Identify the blood parasite species.
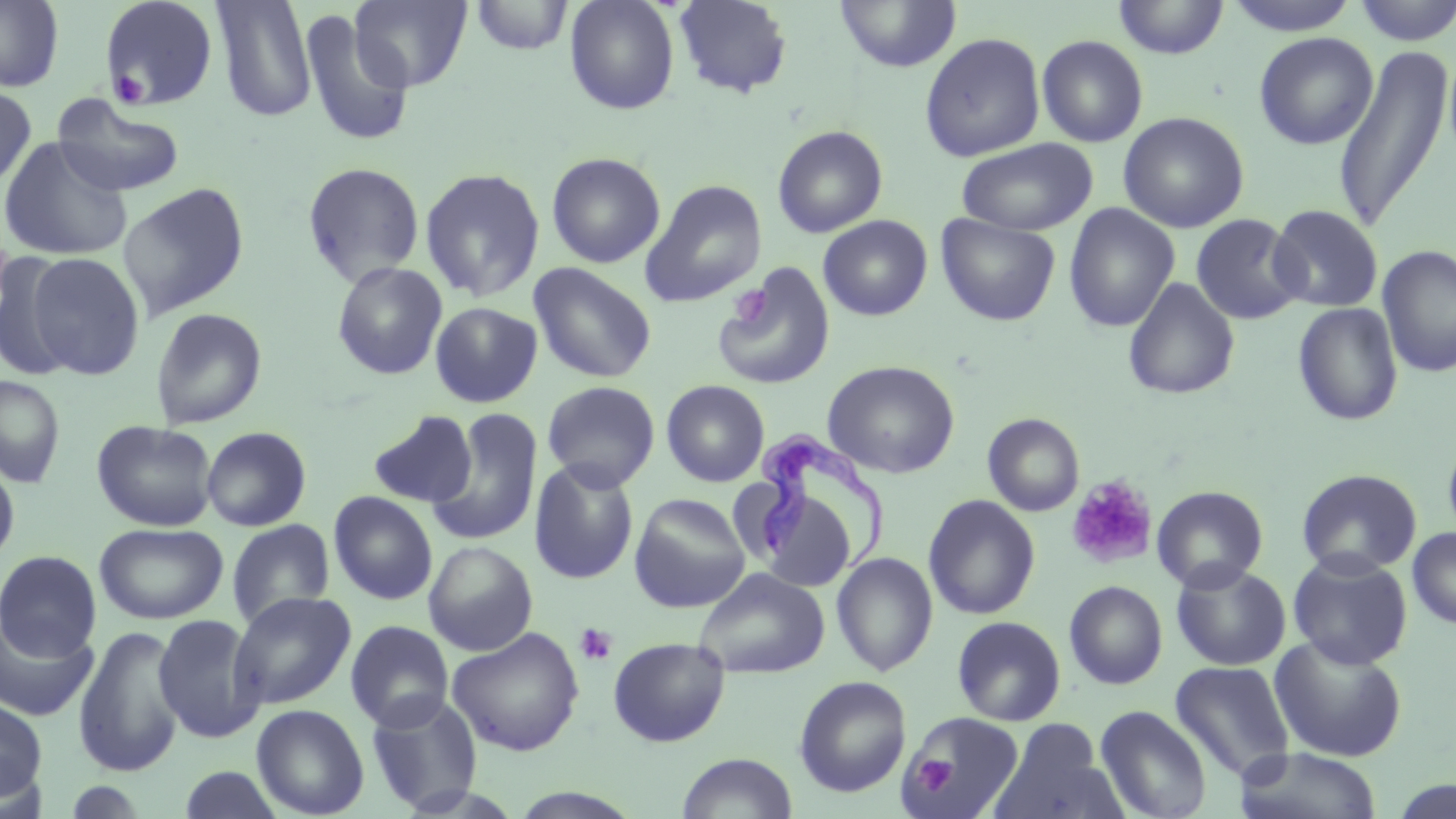
Trypanosoma brucei.

Summary:
  - Coordinate format: approximate bounding boxes as (x1, y1, x2, y2) in pixels
  - Trypanosoma brucei locations: (754, 428, 890, 572)
  - Platelet locations: (108, 66, 150, 108), (729, 285, 770, 327), (1065, 475, 1159, 569), (575, 623, 618, 666), (915, 755, 956, 793)
  - Uninfected red blood cell locations: (0, 0, 64, 92), (99, 0, 219, 110), (350, 0, 472, 92), (469, 0, 573, 56), (564, 0, 680, 115), (673, 0, 793, 99), (1112, 0, 1228, 59), (1222, 0, 1362, 36), (1351, 0, 1455, 46), (211, 1, 316, 122), (834, 1, 962, 73), (297, 9, 415, 149), (919, 32, 1046, 163), (1253, 32, 1378, 150), (1036, 34, 1148, 148), (1332, 41, 1452, 235), (0, 84, 36, 191), (51, 95, 186, 197), (1118, 112, 1250, 233), (772, 125, 888, 237), (0, 137, 133, 262), (956, 138, 1098, 236), (546, 152, 665, 268), (302, 162, 425, 287), (420, 167, 546, 302), (640, 179, 767, 307), (118, 182, 250, 320), (1063, 202, 1180, 333), (1268, 204, 1383, 312), (936, 213, 1060, 326), (1190, 213, 1307, 325), (818, 215, 932, 321), (0, 223, 15, 327), (1377, 244, 1456, 379), (1, 251, 76, 381), (24, 251, 146, 380), (332, 261, 448, 380), (528, 262, 657, 384), (715, 263, 836, 390), (1123, 277, 1240, 400), (430, 302, 542, 407), (1292, 302, 1403, 426), (150, 307, 268, 429), (822, 360, 960, 479), (0, 374, 66, 488), (541, 380, 660, 492), (661, 380, 770, 487), (427, 409, 543, 546), (369, 410, 477, 508), (983, 413, 1084, 517), (91, 419, 218, 531), (201, 426, 312, 531), (1442, 432, 1456, 546), (0, 458, 20, 568), (529, 460, 640, 585), (1296, 468, 1422, 577), (731, 478, 851, 591), (1151, 485, 1268, 593), (328, 491, 438, 605), (629, 493, 751, 613), (923, 494, 1040, 619), (226, 519, 335, 629), (94, 522, 228, 624), (1406, 526, 1456, 630), (423, 540, 538, 655), (0, 550, 102, 660), (1287, 551, 1413, 670), (831, 553, 938, 676), (1171, 560, 1291, 671), (693, 567, 829, 679), (1064, 581, 1168, 690), (229, 591, 357, 709), (0, 613, 98, 722), (152, 613, 266, 743), (951, 616, 1066, 726), (345, 620, 455, 731), (73, 625, 186, 778), (447, 627, 585, 757), (1269, 634, 1408, 762), (608, 637, 730, 747), (1169, 661, 1295, 783), (793, 676, 912, 798), (365, 692, 484, 815), (0, 698, 47, 803), (251, 704, 369, 819), (1094, 705, 1213, 819), (902, 711, 1024, 819), (989, 721, 1123, 819), (1233, 747, 1384, 819), (677, 752, 797, 819), (178, 765, 286, 819)
  - Image size: 1456×819 pixels
  - Modality: light microscopy
  - Preparation: thin blood smear
  - Stain: May-Grünwald-Giemsa
  - Magnification: 1000x
  - Field of view: single